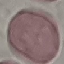
Result: negative for malaria parasites. Giemsa stain. Thin blood smear. Photographed with a smartphone camera at the microscope eyepiece. Cell patch, automatically extracted from a larger field of view and resized to 64 × 64 pixels.